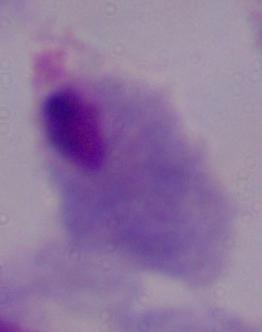
Summary:
  - Modality: photomicrograph
  - Identification: trichomonad
  - Magnification: 1000x